Classify this cell by malaria status.
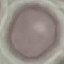

It is uninfected.

preparation = thin blood smear
capture = smartphone camera at the microscope eyepiece
image type = cell patch, automatically extracted from a larger field of view and resized to 64 × 64 pixels
stain = Giemsa